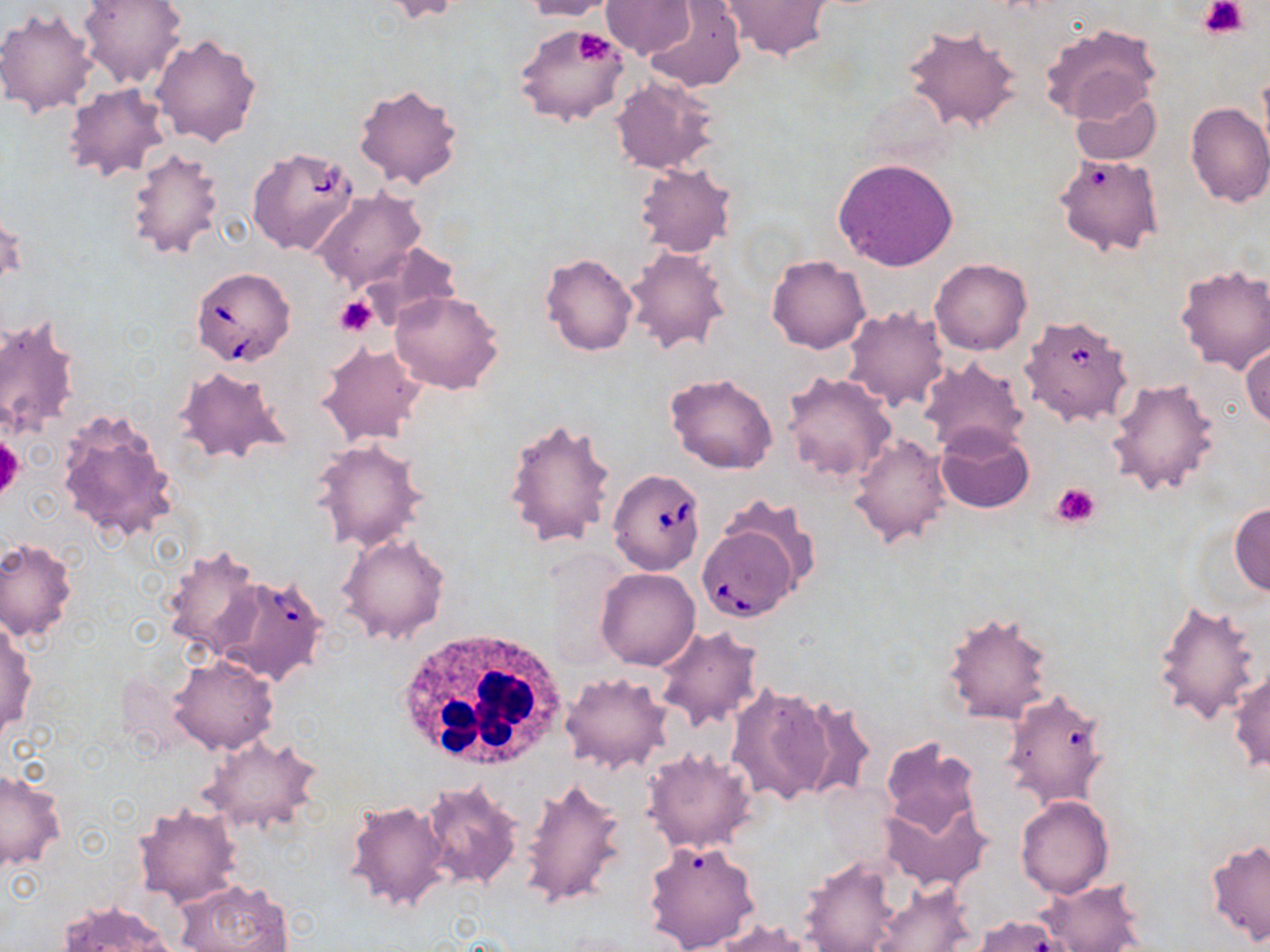
Summary:
  - Coordinate format: approximate bounding boxes as [x1, y1, x2, y2] in pixels
  - Platelet locations: [1199, 0, 1249, 40], [570, 29, 619, 67], [334, 295, 375, 336], [0, 435, 24, 504], [1051, 482, 1101, 528]
  - Uninfected red blood cell locations: [80, 0, 186, 87], [516, 0, 618, 21], [601, 0, 696, 61], [380, 1, 465, 24], [719, 1, 831, 62], [643, 2, 746, 94], [0, 6, 99, 117], [1039, 22, 1161, 126], [515, 25, 632, 128], [901, 25, 1022, 133], [152, 33, 262, 146], [610, 74, 720, 175], [352, 82, 463, 191], [63, 83, 170, 182], [1071, 90, 1161, 166], [1184, 102, 1270, 208], [123, 146, 224, 260], [1053, 153, 1164, 258], [833, 158, 959, 271], [635, 162, 736, 256], [312, 188, 427, 289], [1, 206, 25, 294], [354, 242, 465, 331], [623, 246, 729, 354], [539, 252, 638, 356], [767, 255, 871, 354], [930, 258, 1031, 355], [1175, 263, 1270, 373], [389, 291, 504, 394], [842, 305, 951, 413], [0, 311, 81, 443], [316, 342, 427, 446], [1241, 342, 1269, 432], [918, 357, 1030, 456], [174, 366, 287, 466], [783, 371, 897, 485], [664, 372, 779, 474], [1108, 377, 1222, 496], [56, 409, 180, 542], [503, 417, 619, 549], [934, 426, 1033, 514], [848, 433, 953, 547], [311, 439, 429, 553], [718, 494, 822, 595], [1230, 500, 1270, 596], [337, 532, 451, 645], [0, 538, 77, 643], [161, 546, 264, 658], [594, 567, 701, 670], [1150, 597, 1264, 725], [941, 610, 1055, 724], [1, 619, 37, 740], [653, 624, 764, 731], [169, 654, 277, 754], [1228, 668, 1270, 774], [561, 672, 672, 775], [727, 681, 835, 806], [1000, 687, 1113, 810], [791, 696, 878, 803], [201, 733, 324, 837], [879, 736, 982, 840], [641, 747, 759, 855], [0, 768, 65, 874], [519, 775, 630, 912], [420, 781, 524, 890], [882, 795, 993, 893], [1016, 796, 1115, 898], [344, 799, 451, 914], [132, 801, 242, 907], [644, 839, 762, 952], [1205, 839, 1269, 949], [799, 855, 905, 952], [176, 878, 291, 952], [1037, 878, 1147, 952], [870, 880, 977, 952], [54, 900, 179, 951], [974, 914, 1072, 952], [708, 919, 817, 951]
  - White blood cell locations: [392, 626, 568, 774]
  - Babesia divergens-infected red blood cell locations: [247, 146, 359, 256], [190, 266, 296, 366], [1018, 313, 1137, 429], [607, 471, 704, 574], [697, 523, 800, 621], [210, 572, 329, 687]
  - Slide-level diagnosis: Babesia divergens
  - Field of view: one of a larger specimen
  - Preparation: thin blood smear
  - Magnification: 1000x
  - Stain: May-Grünwald-Giemsa
  - Image size: 1270×952 pixels
  - Modality: optical microscopy